Identify the preparation type.
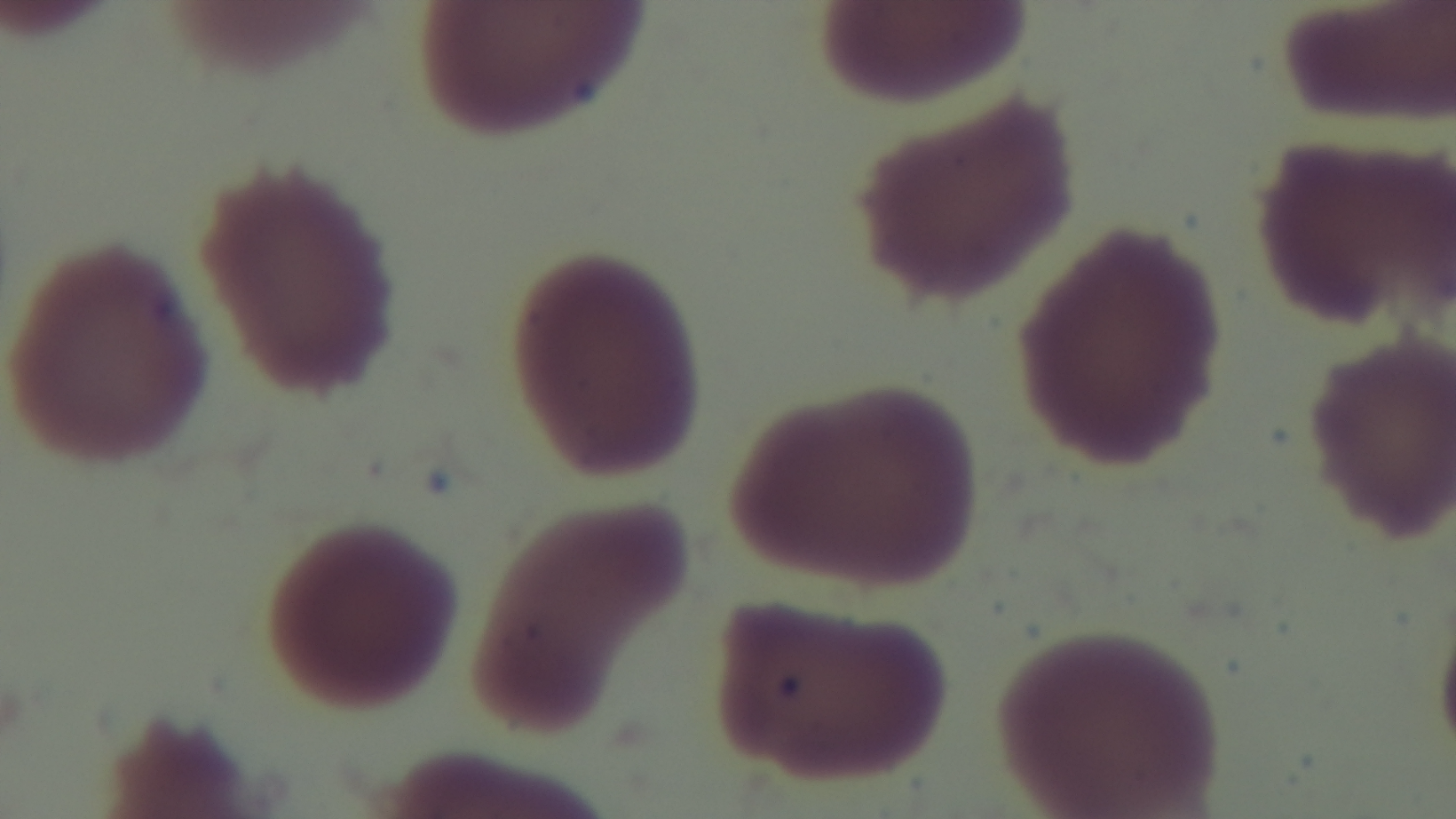
Thin.

malaria status = negative
capture = mounted 4K digital camera
stain = Giemsa
modality = light microscopy
field of view = one from the slide
objective = 100x oil immersion